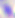
Photomicrograph. 400x magnification. Toxoplasma gondii is seen.